Report the malaria status of this cell.
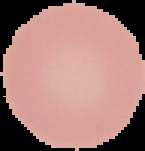

It is uninfected.

Summary:
  - Image type: segmented cell region with the area outside set to black
  - Preparation: thin blood film
  - Image size: 145×151 pixels